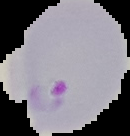
image type = segmented cell region on a black background
image size = 130×136 pixels
result = malaria parasites detected
preparation = thin blood smear